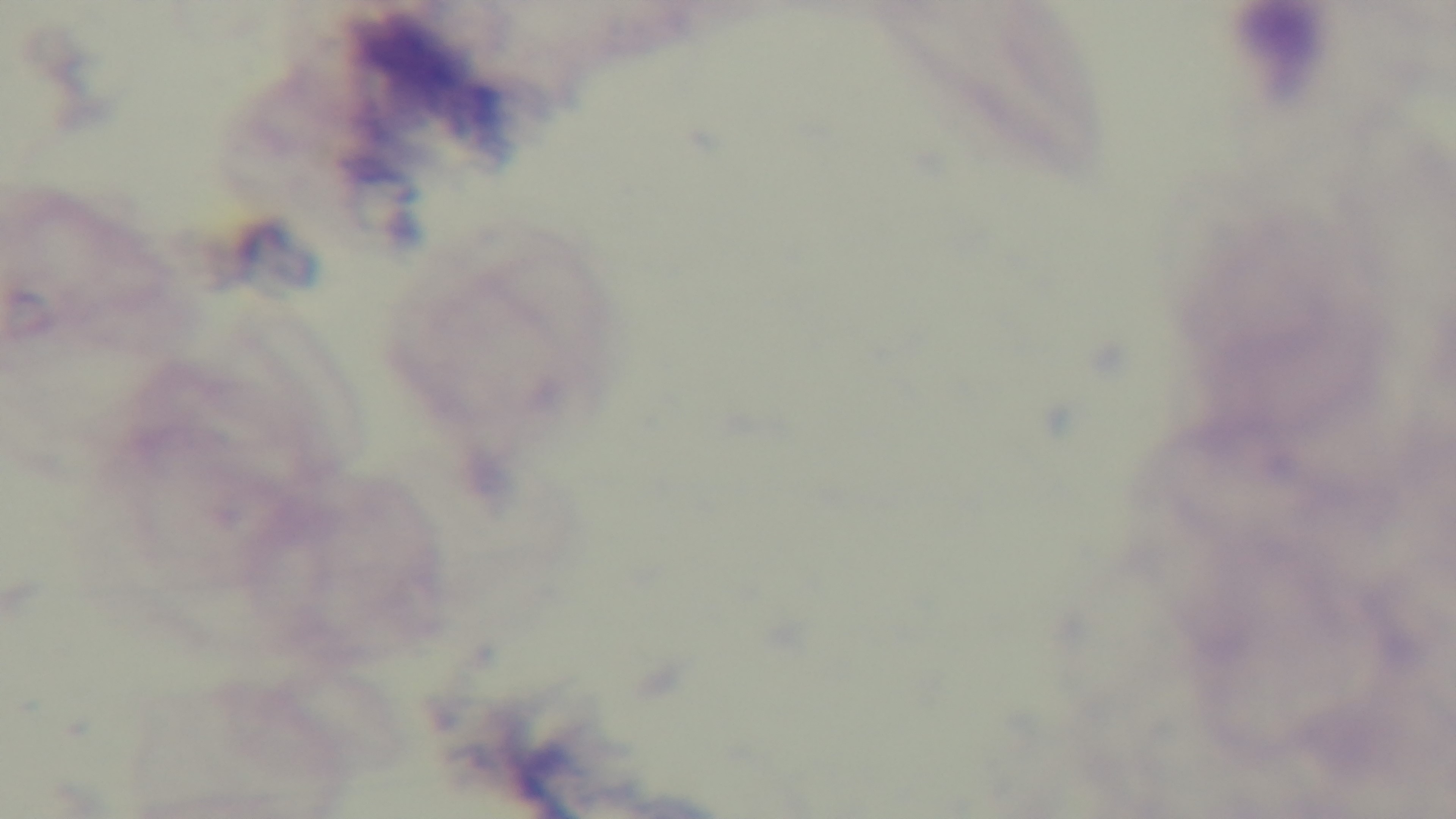

Preparation: thick. Mounted 4K digital camera. Malaria status: negative. Light microscopy. 100x oil-immersion objective. Giemsa stain. Single field of view.